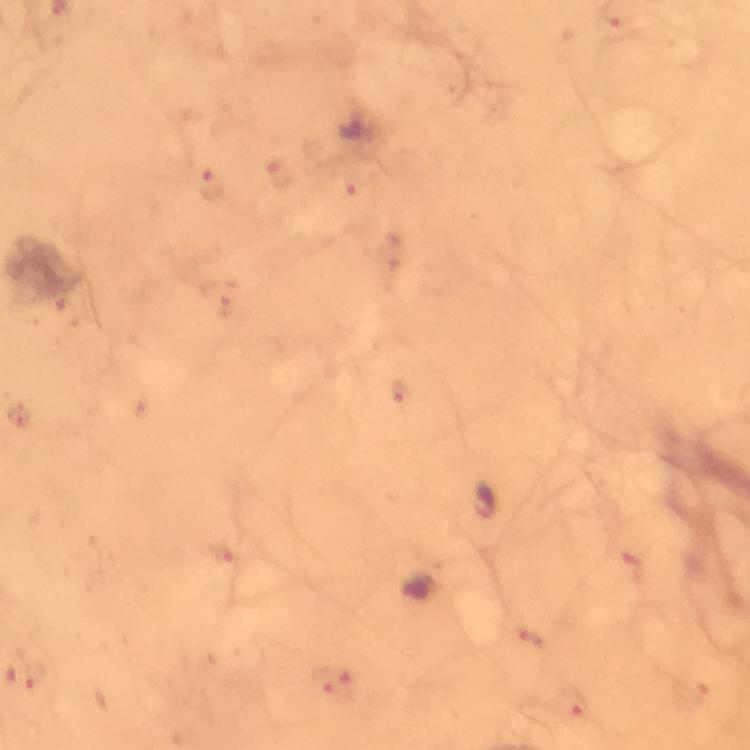

Approximate centers as {x, y} in pixels.
Summary:
  - Malaria parasite locations: {211, 189}
  - Capture: smartphone mounted on the microscope
  - Image size: 750×750 pixels
  - Magnification: 100x
  - Context: from a diagnostic examination for malaria
  - Cropped from: one field of view
  - Preparation: thick smear
  - Immersion oil: used
  - Stain: Giemsa